Name the parasite shown.
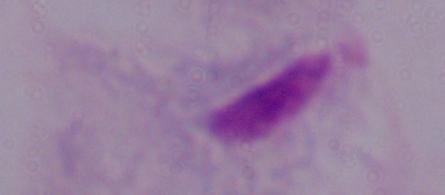

This is a trichomonad.

Micrograph. Captured at 1000x magnification.